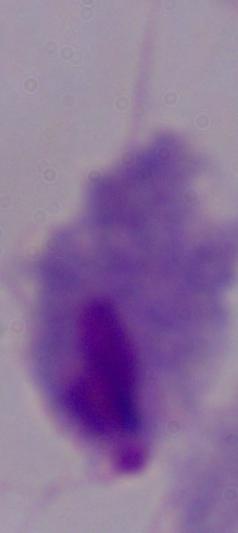

Captured at 1000x magnification. A trichomonad is shown. Micrograph.